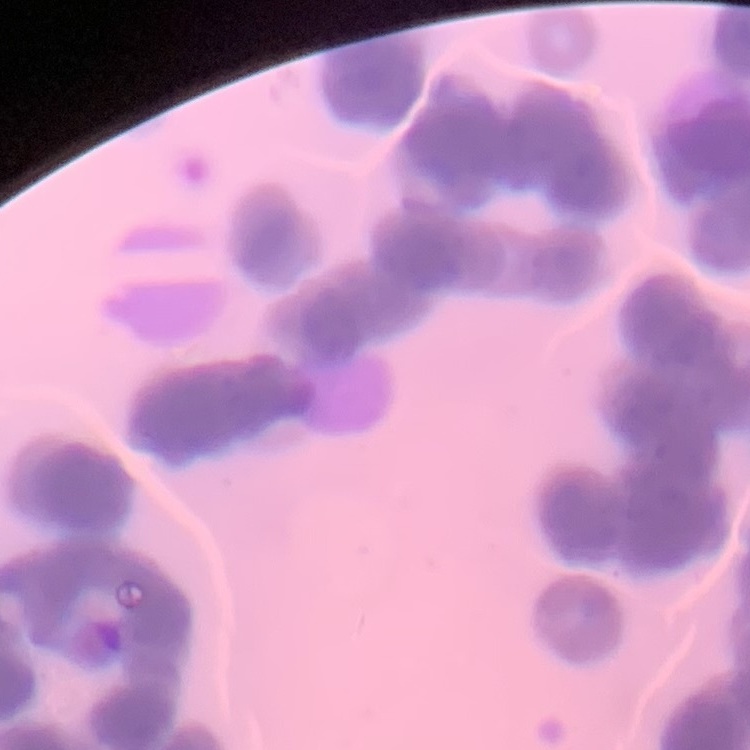

Summary:
  - Erythrocyte morphology: rouleaux formation
  - Stain: Field's or Giemsa
  - Preparation: thin peripheral smear
  - Image type: square crop of a larger photomicrograph